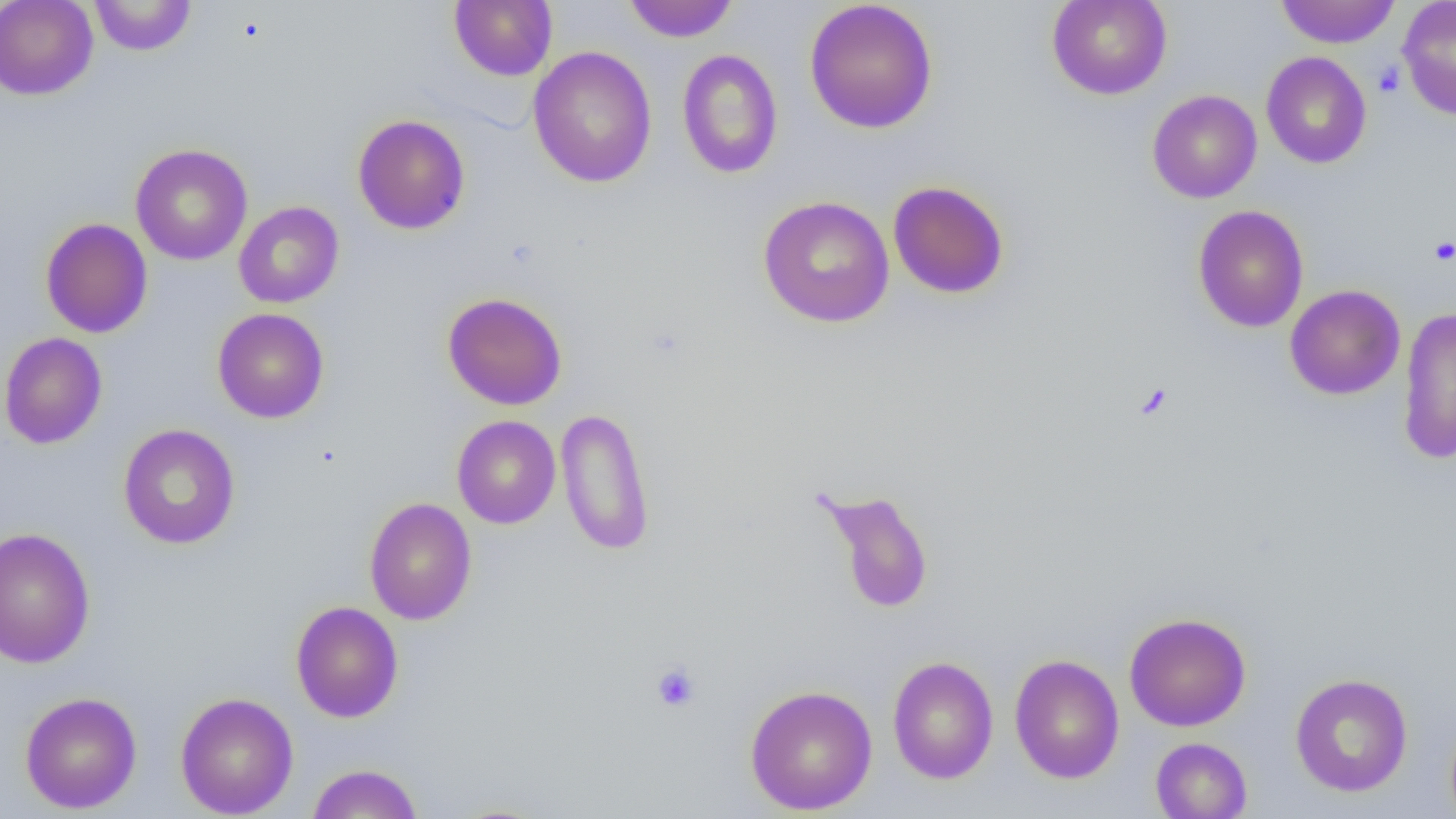
slide_level_diagnosis: no evidence of blood parasites
modality: light microscopy
platelet_locations: 'approximate bounding boxes as [x1, y1, x2, y2] in pixels: [1373, 61, 1405, 97], [1429, 236, 1456, 265], [650, 661, 701, 713]'
uninfected_red_blood_cell_locations: 'approximate bounding boxes as [x1, y1, x2, y2] in pixels: [0, 0, 98, 100], [89, 0, 196, 56], [449, 0, 557, 81], [623, 0, 738, 42], [804, 0, 938, 134], [1046, 0, 1172, 100], [1275, 0, 1400, 48], [1397, 0, 1456, 120], [528, 46, 657, 188], [677, 48, 783, 179], [1261, 51, 1372, 169], [1147, 89, 1262, 203], [352, 114, 471, 235], [130, 143, 252, 265], [887, 180, 1010, 299], [758, 196, 895, 328], [233, 201, 344, 308], [1192, 205, 1309, 333], [40, 218, 153, 338], [1285, 284, 1405, 400], [442, 292, 568, 410], [1397, 307, 1456, 464], [212, 308, 329, 423], [0, 332, 107, 449], [555, 406, 656, 557], [452, 415, 561, 529], [117, 423, 240, 549], [818, 487, 935, 615], [364, 498, 477, 625], [0, 526, 96, 668], [290, 601, 403, 723], [1123, 612, 1251, 732], [1009, 653, 1124, 784], [887, 655, 999, 784], [1290, 673, 1413, 797], [744, 684, 878, 815], [19, 691, 142, 814], [175, 691, 299, 818], [1150, 737, 1252, 818], [307, 763, 423, 819]'
field_of_view: single
image_size: 1456×819 pixels
preparation: thin blood smear
magnification: 1000x